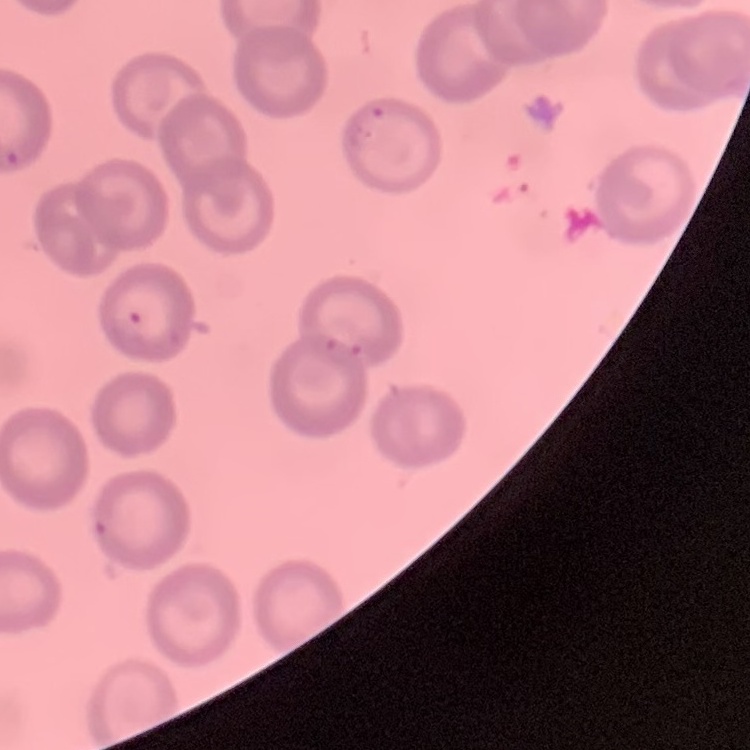
{
  "red_blood_cell_morphology": "no rouleaux formation",
  "stain": "Field's or Giemsa",
  "image_type": "square crop of a larger photomicrograph",
  "preparation": "thin blood film"
}